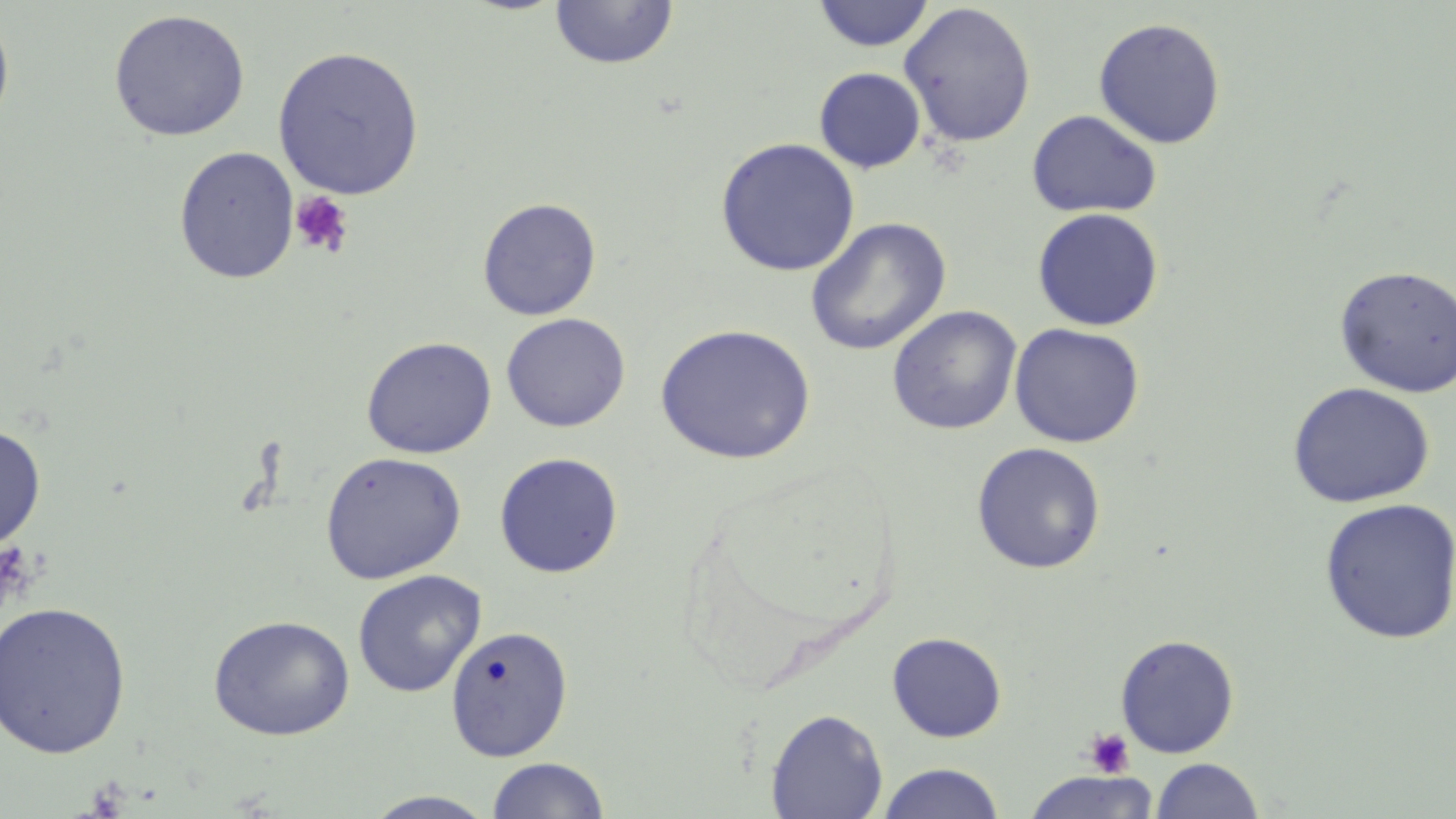
Summary:
  - Coordinate format: approximate bounding boxes as named x1/y1/x2/y2 corners in pixels
  - Uninfected red blood cell locations: (x1=812, y1=0, x2=935, y2=52), (x1=549, y1=1, x2=679, y2=70), (x1=898, y1=2, x2=1037, y2=149), (x1=0, y1=8, x2=15, y2=141), (x1=108, y1=9, x2=250, y2=142), (x1=1093, y1=17, x2=1227, y2=149), (x1=272, y1=46, x2=425, y2=200), (x1=814, y1=67, x2=926, y2=173), (x1=1026, y1=109, x2=1162, y2=218), (x1=715, y1=137, x2=860, y2=277), (x1=173, y1=146, x2=299, y2=284), (x1=477, y1=197, x2=602, y2=321), (x1=1032, y1=207, x2=1164, y2=331), (x1=804, y1=217, x2=952, y2=356), (x1=1334, y1=264, x2=1456, y2=397), (x1=887, y1=305, x2=1022, y2=435), (x1=500, y1=312, x2=631, y2=432), (x1=1009, y1=322, x2=1145, y2=448), (x1=655, y1=323, x2=816, y2=465), (x1=361, y1=336, x2=497, y2=459), (x1=1287, y1=381, x2=1435, y2=509), (x1=0, y1=423, x2=46, y2=551), (x1=971, y1=441, x2=1106, y2=574), (x1=320, y1=451, x2=467, y2=584), (x1=494, y1=452, x2=624, y2=578), (x1=1319, y1=498, x2=1456, y2=645), (x1=352, y1=569, x2=486, y2=698), (x1=0, y1=600, x2=132, y2=760), (x1=208, y1=614, x2=355, y2=741), (x1=446, y1=624, x2=573, y2=762), (x1=887, y1=632, x2=1007, y2=742), (x1=1115, y1=633, x2=1240, y2=758), (x1=765, y1=708, x2=888, y2=819), (x1=486, y1=757, x2=611, y2=818), (x1=1150, y1=758, x2=1264, y2=818), (x1=877, y1=762, x2=1005, y2=819), (x1=1021, y1=771, x2=1161, y2=819), (x1=362, y1=790, x2=499, y2=818)
  - Platelet locations: (x1=289, y1=191, x2=354, y2=259), (x1=0, y1=540, x2=36, y2=619), (x1=1084, y1=728, x2=1136, y2=778)
  - Slide-level diagnosis: negative for blood parasites
  - Modality: optical microscopy
  - Magnification: 1000x
  - Stain: May-Grünwald-Giemsa
  - Preparation: thin blood film
  - Field of view: single
  - Image size: 1456×819 pixels